Locate every blood parasite and identify its species.
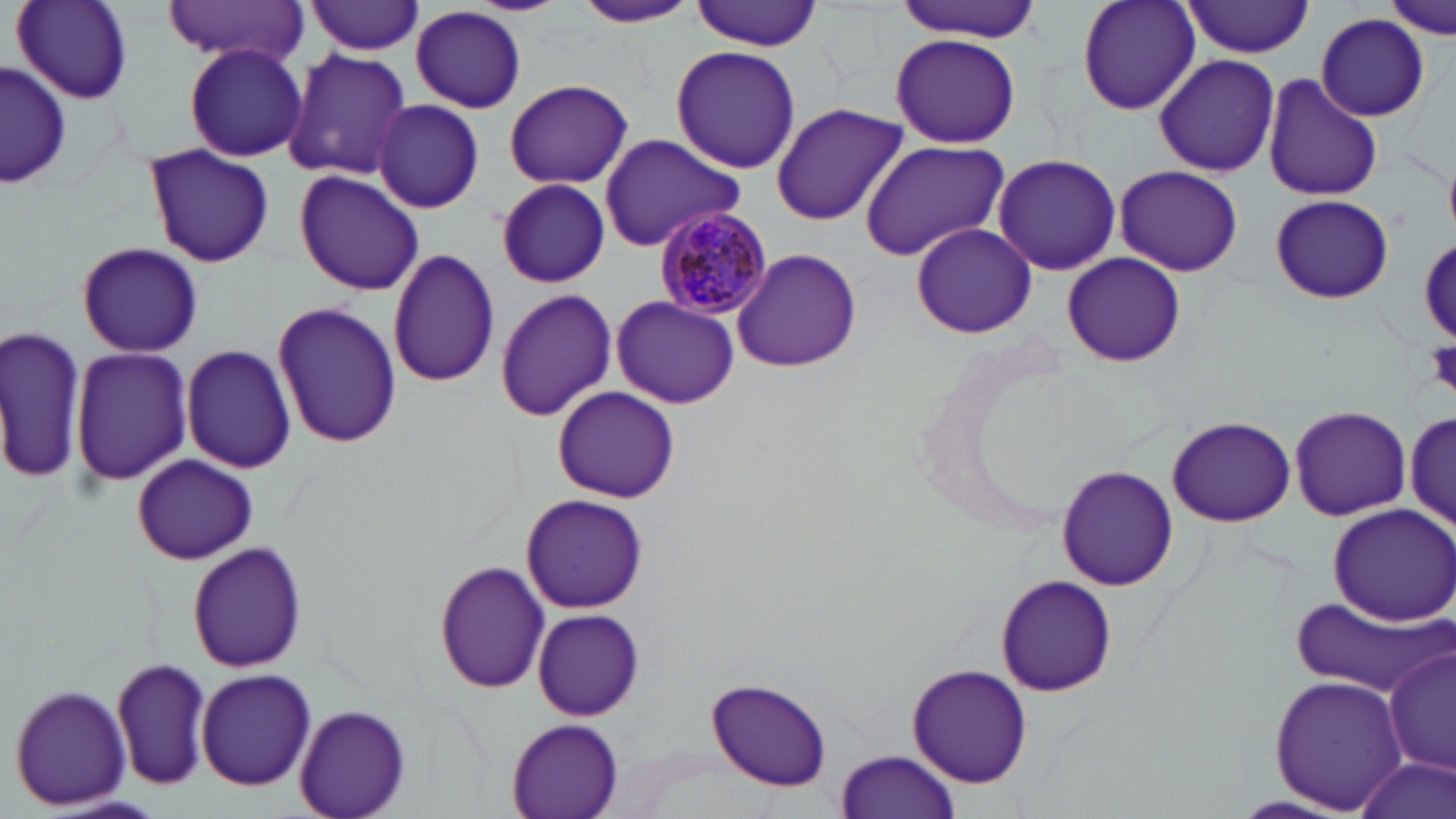
Approximate bounding boxes as (x1, y1, x2, y2) in pixels.
Plasmodium malariae-infected red blood cells: (654, 208, 776, 321).
No Plasmodium falciparum, Plasmodium ovale, Plasmodium vivax, Babesia divergens, or Trypanosoma brucei observed.

Summary:
  - Platelet locations: (1423, 339, 1456, 395)
  - Uninfected red blood cell locations: (163, 0, 308, 63), (306, 0, 426, 55), (693, 0, 822, 51), (891, 0, 1043, 43), (1075, 0, 1203, 116), (1386, 0, 1453, 38), (12, 1, 135, 106), (576, 1, 698, 31), (1180, 2, 1315, 57), (410, 7, 528, 113), (1317, 14, 1429, 120), (1080, 19, 1244, 161), (888, 33, 1023, 150), (183, 42, 307, 162), (669, 46, 802, 175), (283, 49, 410, 178), (1153, 55, 1281, 177), (1, 61, 71, 192), (1260, 74, 1383, 203), (501, 76, 635, 188), (372, 99, 483, 213), (769, 102, 910, 226), (599, 133, 747, 249), (859, 140, 1011, 261), (144, 142, 273, 269), (992, 153, 1122, 276), (1115, 165, 1243, 275), (294, 169, 425, 296), (495, 177, 612, 288), (1270, 195, 1394, 305), (908, 221, 1039, 340), (74, 242, 205, 357), (732, 246, 862, 373), (387, 247, 503, 389), (1062, 251, 1185, 369), (494, 285, 618, 424), (610, 295, 738, 409), (270, 300, 402, 450), (0, 321, 85, 484), (181, 344, 297, 474), (70, 347, 193, 488), (549, 386, 681, 503), (1289, 405, 1411, 521), (1407, 405, 1455, 534), (1167, 415, 1295, 528), (132, 453, 258, 565), (1056, 462, 1177, 592), (520, 495, 649, 614), (1326, 502, 1456, 626), (186, 538, 306, 673), (434, 559, 551, 694), (995, 573, 1117, 699), (1294, 598, 1451, 699), (531, 608, 645, 721), (1385, 647, 1455, 776), (112, 656, 213, 792), (906, 661, 1032, 791), (195, 668, 316, 791), (1268, 673, 1408, 815), (704, 677, 832, 791), (8, 682, 132, 812), (294, 704, 411, 819), (506, 715, 627, 819), (835, 750, 961, 819), (1350, 754, 1453, 819)
  - Slide-level diagnosis: Plasmodium malariae
  - Field of view: single
  - Stain: May-Grünwald-Giemsa
  - Preparation: thin blood film
  - Image size: 1456×819 pixels
  - Modality: optical microscopy
  - Magnification: 1000x